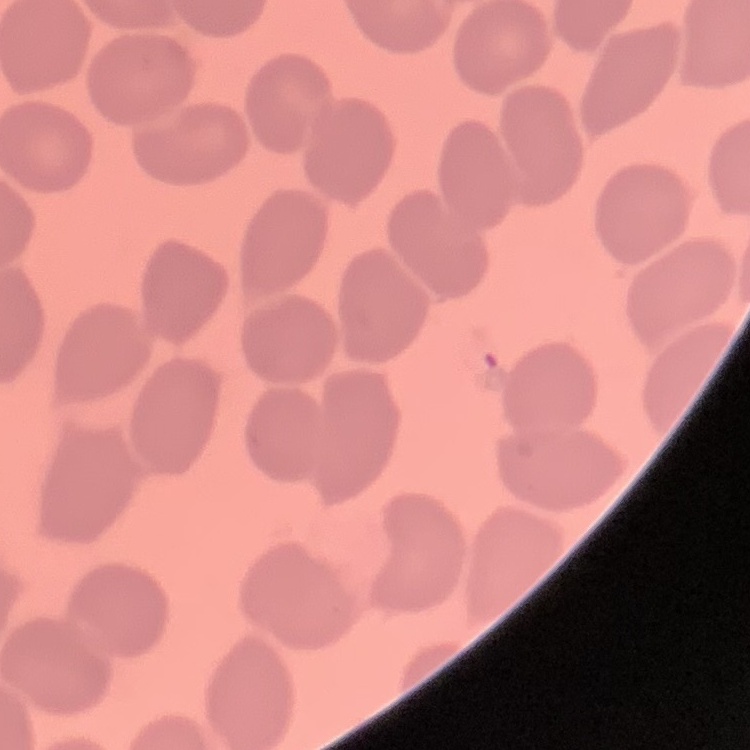

The red blood cells exhibit no rouleaux formation. Field's or Giemsa stain. Square crop of a larger photomicrograph. Thin blood smear.